Report the malaria status of this cell.
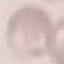
Uninfected.

stain: Giemsa
capture: smartphone camera at the microscope eyepiece
preparation: thin blood smear
image_type: cell patch, automatically extracted from a larger field of view and resized to 64 × 64 pixels